Locate every blood parasite and identify its species.
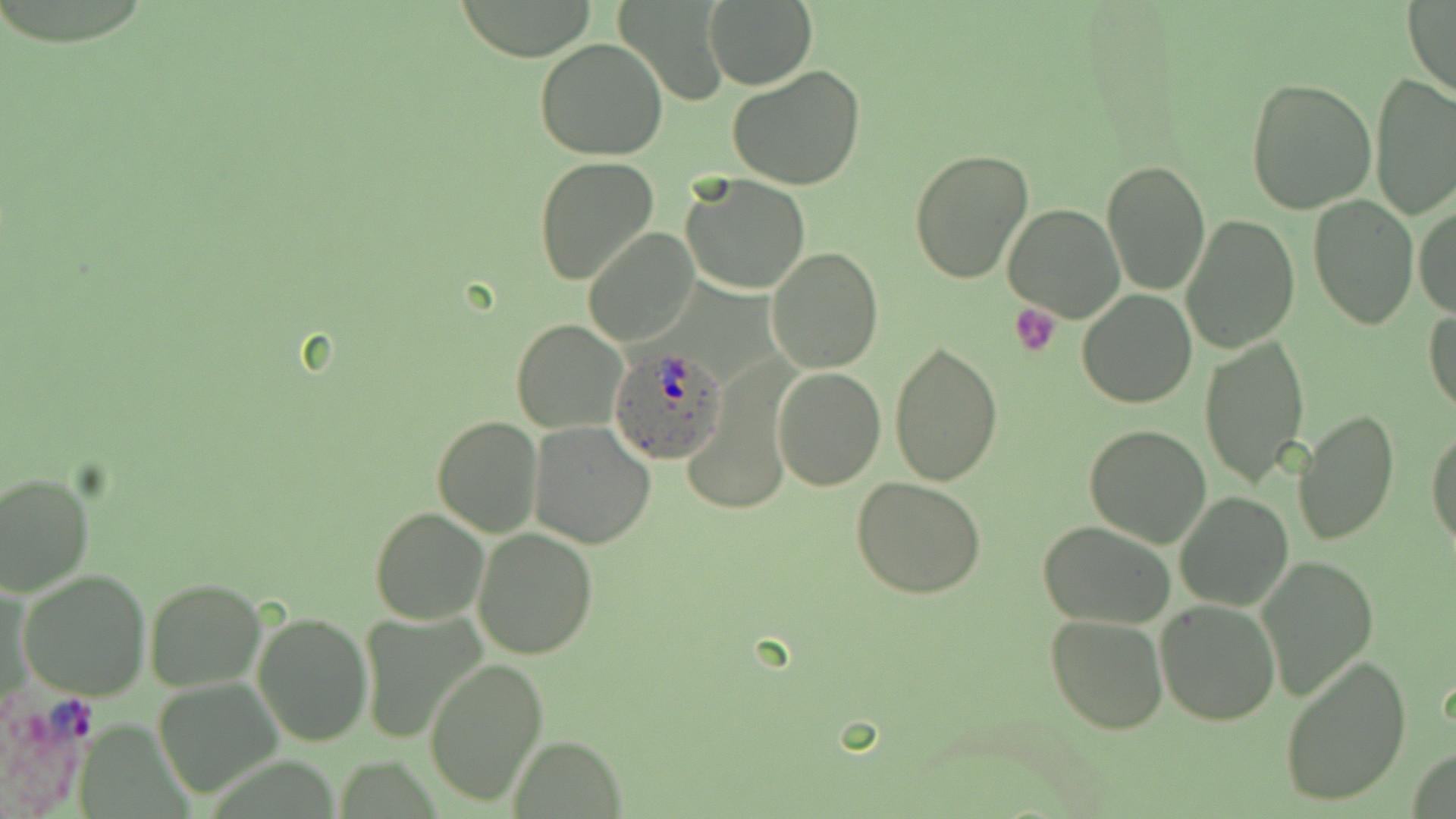

Approximate bounding boxes as (x1,y1)-(x2,y2) corner pairs in pixels.
Plasmodium ovale-infected red blood cells: (610,344)-(729,462).
No Plasmodium falciparum, Plasmodium malariae, Plasmodium vivax, Babesia divergens, or Trypanosoma brucei observed.

Summary:
  - Platelet locations: (1009,303)-(1060,357)
  - Uninfected red blood cell locations: (615,0)-(728,106), (702,0)-(818,90), (457,1)-(599,60), (1403,1)-(1456,101), (535,37)-(668,161), (728,65)-(866,191), (1370,73)-(1456,220), (1245,77)-(1376,215), (907,148)-(1034,284), (534,157)-(659,287), (1100,160)-(1210,296), (680,174)-(810,294), (1309,196)-(1417,329), (1002,201)-(1126,322), (1413,204)-(1456,320), (1180,214)-(1301,354), (584,227)-(699,348), (769,247)-(882,371), (1076,289)-(1198,408), (1424,307)-(1456,417), (510,320)-(627,434), (1200,335)-(1310,487), (888,341)-(1002,486), (772,366)-(886,491), (1294,408)-(1399,547), (430,415)-(543,537), (528,421)-(658,550), (1084,423)-(1214,549), (1427,424)-(1456,552), (0,470)-(94,597), (852,477)-(987,600), (1173,490)-(1293,613), (370,507)-(488,624), (368,517)-(595,637), (1039,521)-(1174,629), (472,528)-(598,661), (1258,557)-(1379,699), (17,569)-(152,700), (144,577)-(267,694), (1155,599)-(1280,726), (252,610)-(374,747), (358,611)-(485,740), (1045,612)-(1167,734), (1277,654)-(1412,808), (424,657)-(547,807), (154,677)-(282,799), (512,735)-(624,817), (1407,746)-(1454,819)
  - Slide-level diagnosis: Plasmodium ovale
  - Magnification: 1000x
  - Field of view: one of a larger specimen
  - Image size: 1456×819 pixels
  - Preparation: thin blood smear
  - Modality: optical microscopy
  - Stain: May-Grünwald-Giemsa